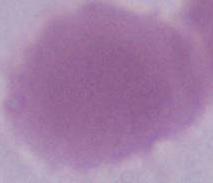

identification = red blood cell
modality = photomicrograph
magnification = 1000x